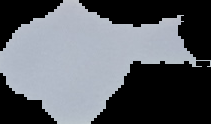

Cell region segmented out of the field of view; the surrounding area is masked to black. Malaria status: uninfected. Image is 211×124 pixels. From a thin blood film.